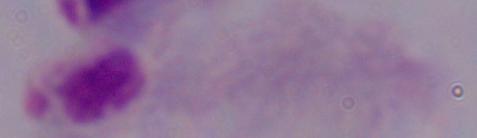
1000x magnification. Micrograph. A trichomonad is shown.